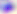

modality = photomicrograph
identification = Toxoplasma gondii
magnification = 400x